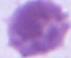 A red blood cell is shown. Captured at 1000x magnification. Micrograph.